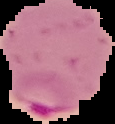
Summary:
  - Image size: 115×124 pixels
  - Image type: cell region segmented out of the field of view; surrounding area masked to black
  - Malaria status: parasitized
  - Preparation: thin blood film